Assess the morphology of the red blood cells.
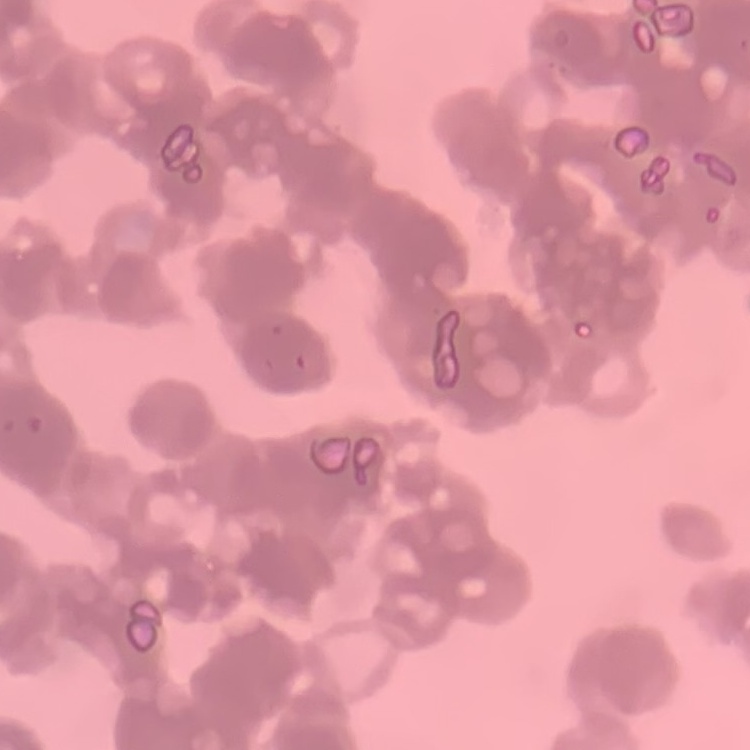

They show rouleaux formation.

Summary:
  - Image type: square crop of a larger photomicrograph
  - Stain: Field's or Giemsa
  - Preparation: thin peripheral smear